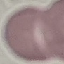

Summary:
  - Malaria status: uninfected
  - Capture: smartphone camera at the microscope eyepiece
  - Preparation: thin smear
  - Image type: automatically extracted cell patch, resized to 64 × 64 pixels
  - Stain: Giemsa